Assess the morphology of the erythrocytes.
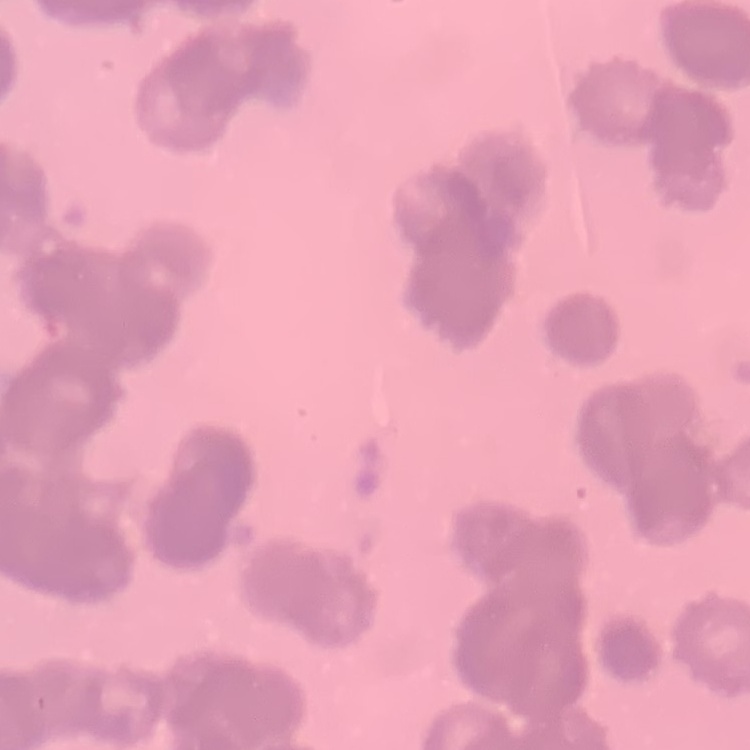
Rouleaux formation.

Field's or Giemsa stain. Thin blood smear. One tile cut from a larger photomicrograph.